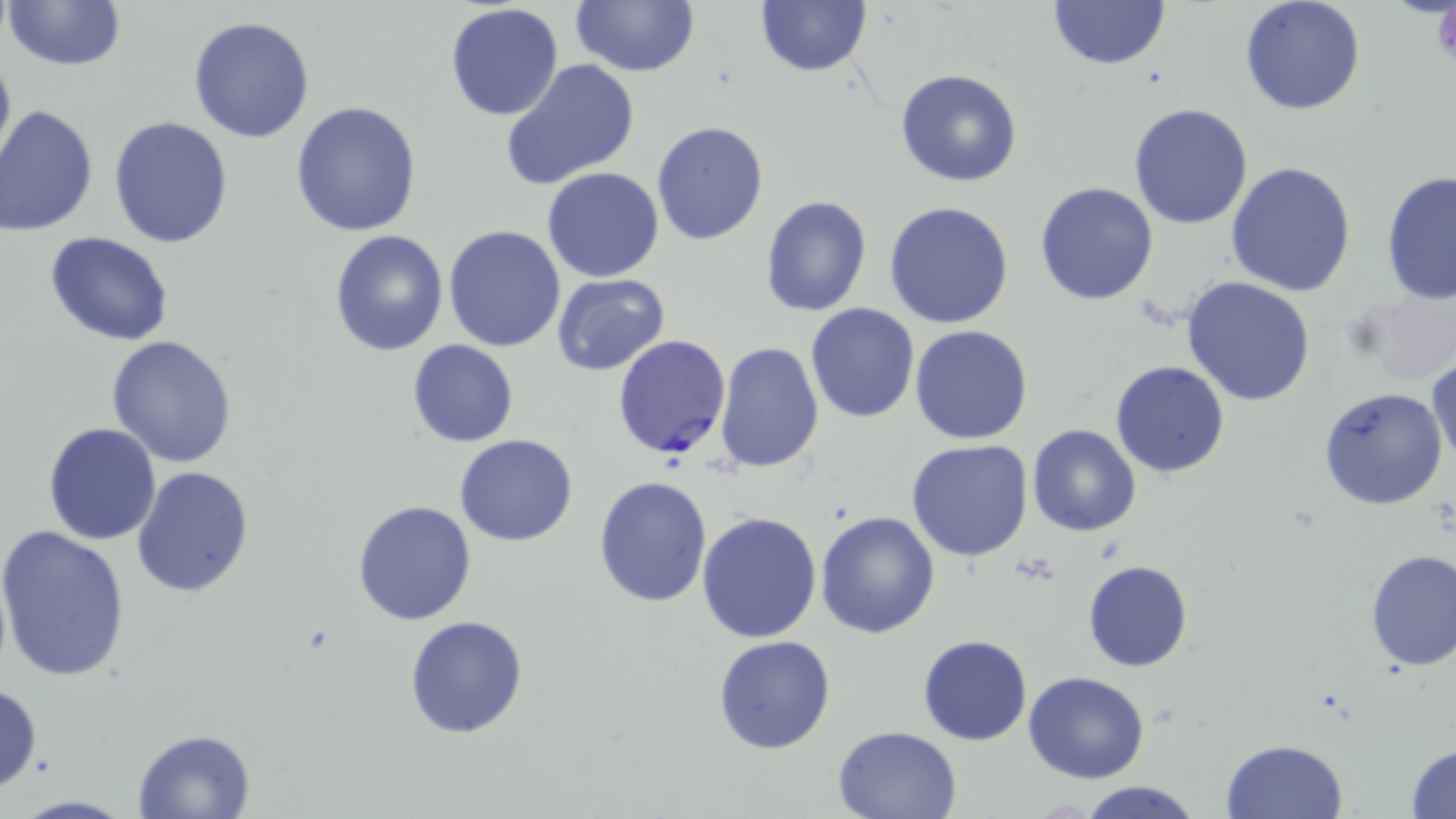
Summary:
  - Coordinate format: approximate bounding boxes as [x1, y1, x2, y2] in pixels
  - Uninfected red blood cell locations: [4, 0, 127, 74], [1048, 0, 1169, 70], [1239, 0, 1366, 115], [570, 1, 700, 77], [753, 1, 873, 77], [444, 3, 564, 121], [187, 15, 315, 142], [0, 42, 16, 173], [501, 58, 639, 189], [895, 68, 1023, 187], [290, 100, 423, 236], [1128, 104, 1255, 230], [0, 106, 99, 236], [109, 116, 234, 249], [651, 121, 770, 246], [1225, 161, 1356, 296], [541, 167, 665, 283], [1380, 169, 1456, 307], [1035, 181, 1159, 305], [760, 195, 872, 317], [884, 200, 1015, 329], [443, 225, 565, 354], [329, 230, 448, 356], [46, 233, 175, 347], [551, 273, 670, 377], [1180, 277, 1318, 407], [1350, 288, 1456, 385], [804, 302, 920, 424], [714, 321, 918, 451], [909, 324, 1033, 445], [106, 335, 238, 468], [407, 339, 519, 448], [715, 341, 825, 471], [1429, 358, 1456, 469], [1109, 360, 1231, 478], [1318, 386, 1448, 510], [42, 422, 163, 545], [1027, 423, 1141, 537], [455, 434, 579, 546], [906, 439, 1033, 562], [132, 464, 256, 598], [593, 474, 712, 609], [351, 499, 476, 625], [816, 511, 940, 640], [696, 512, 823, 644], [0, 525, 132, 682], [1363, 549, 1455, 672], [1082, 560, 1193, 671], [405, 615, 529, 738], [917, 634, 1033, 745], [713, 635, 835, 753], [1023, 672, 1149, 784], [0, 683, 44, 792], [833, 725, 961, 818], [132, 728, 257, 818], [1221, 739, 1348, 819], [1407, 742, 1456, 818], [1077, 781, 1203, 819]
  - Platelet locations: [1427, 6, 1455, 68]
  - Plasmodium falciparum-infected red blood cell locations: [612, 335, 731, 459]
  - Slide-level diagnosis: Plasmodium falciparum
  - Modality: light microscopy
  - Field of view: single
  - Image size: 1456×819 pixels
  - Magnification: 1000x
  - Stain: May-Grünwald-Giemsa
  - Preparation: thin blood smear